Report the malaria status of this cell.
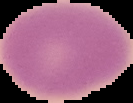

Uninfected.

image type = segmented cell region with the area outside set to black
preparation = thin blood smear
image size = 133×103 pixels